Comment on the morphology of the erythrocytes.
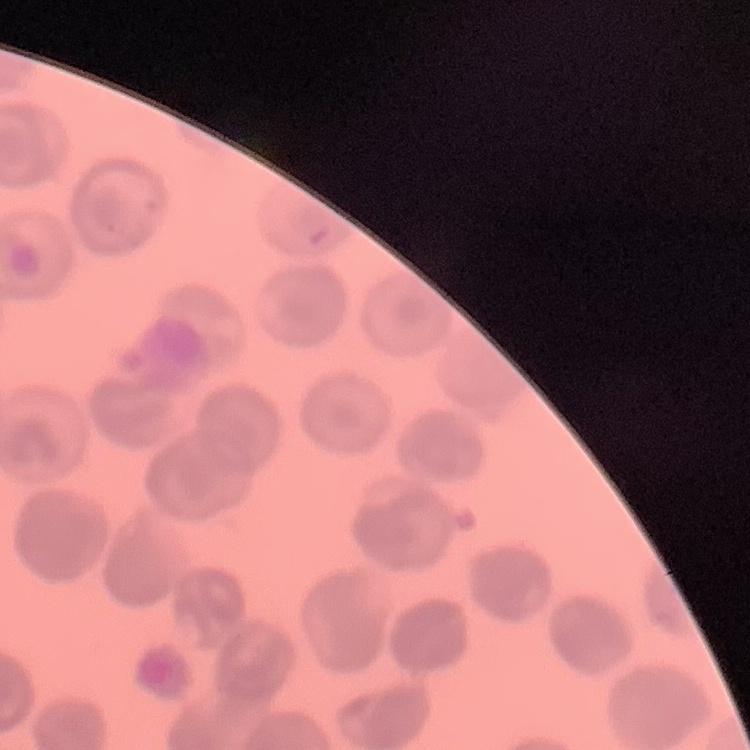
No rouleaux formation.

Square crop of a larger photomicrograph. Thin blood smear. Field's or Giemsa stain.